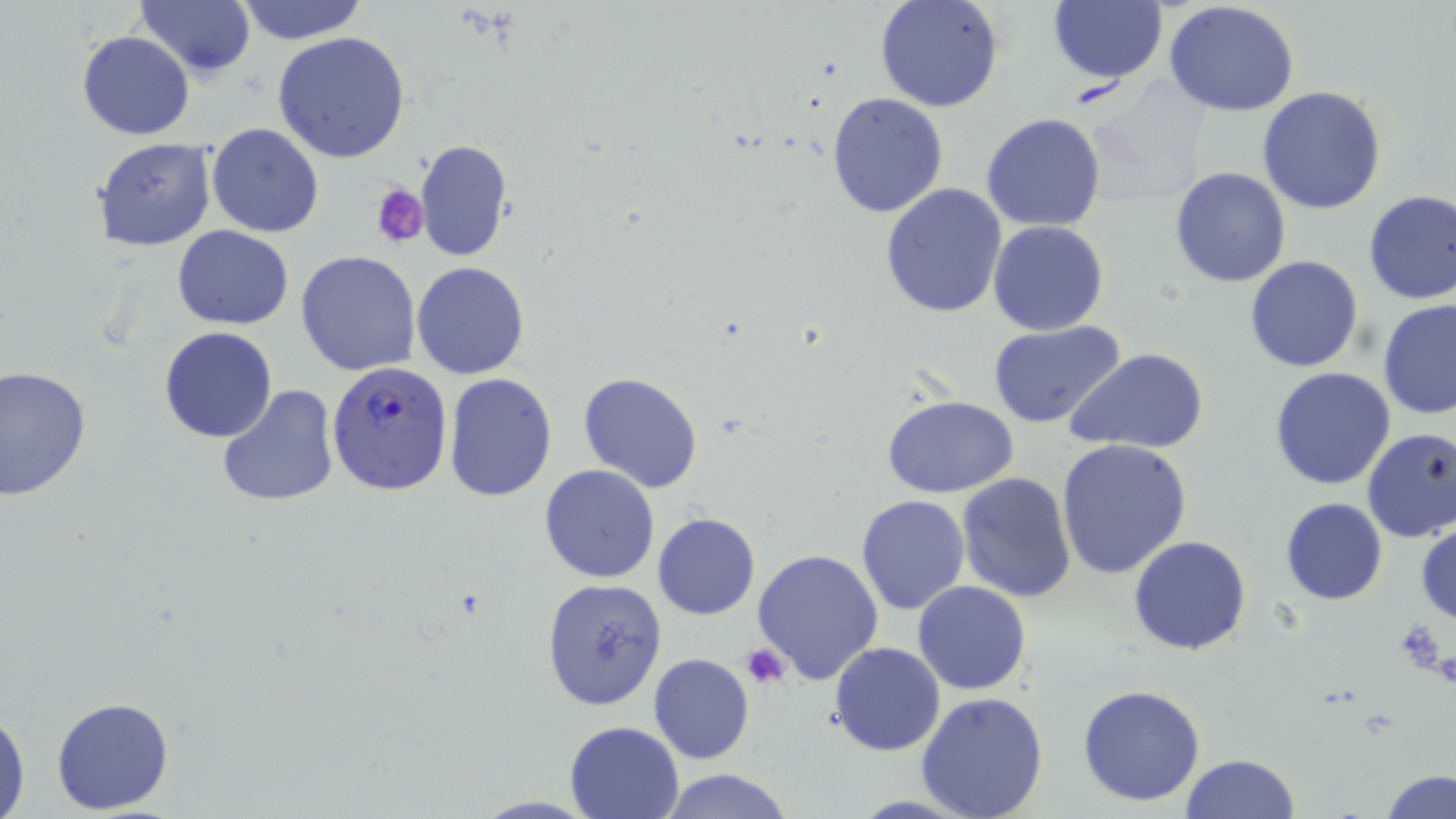
Approximate bounding boxes as (x1,y1)-(x2,y2) corner pairs in pixels. Uninfected red blood cell locations: (233,0)-(369,45), (874,0)-(1005,113), (135,1)-(256,80), (1163,1)-(1302,116), (1047,2)-(1168,84), (77,31)-(195,141), (272,31)-(410,162), (1257,86)-(1387,214), (825,92)-(950,218), (981,112)-(1106,234), (206,124)-(324,238), (92,136)-(216,250), (414,139)-(513,263), (1169,167)-(1292,288), (879,182)-(1008,320), (1362,189)-(1456,305), (989,220)-(1109,335), (172,227)-(293,328), (297,251)-(421,375), (1244,255)-(1364,373), (410,262)-(530,380), (1377,299)-(1456,420), (989,321)-(1124,429), (158,327)-(277,443), (1067,349)-(1208,455), (0,366)-(91,500), (1269,368)-(1396,490), (443,372)-(558,502), (578,372)-(703,494), (216,384)-(340,507), (881,393)-(1019,498), (1360,428)-(1456,543), (1055,439)-(1192,580), (540,464)-(662,583), (956,473)-(1076,602), (854,494)-(970,616), (1280,498)-(1387,605), (653,513)-(759,620), (1415,518)-(1456,626), (1129,535)-(1251,657), (754,549)-(885,685), (542,579)-(668,710), (913,581)-(1031,695), (828,641)-(945,756), (649,654)-(755,764), (1078,683)-(1204,806), (914,692)-(1050,819), (49,695)-(175,813), (0,704)-(30,819), (563,720)-(686,818), (1180,754)-(1301,819), (659,768)-(796,819), (1379,769)-(1456,819). Plasmodium falciparum-infected red blood cell locations: (327,359)-(454,494). Platelet locations: (371,183)-(427,248), (1391,616)-(1451,676), (742,643)-(792,688). Slide-level diagnosis: Plasmodium falciparum. May-Grünwald-Giemsa-stained preparation. Single field of view. 1000x magnification. Thin blood smear. Optical microscopy. Image is 1456×819 pixels.